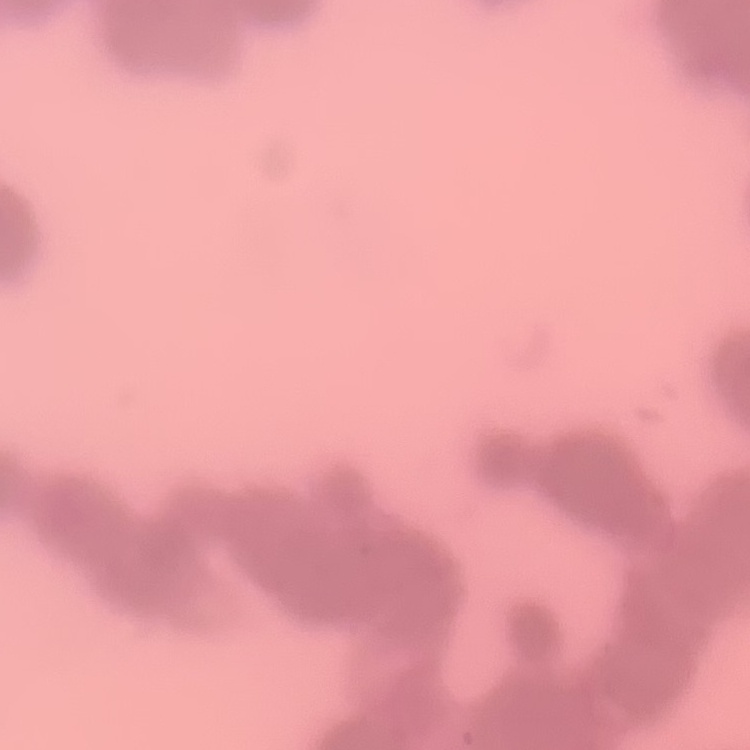

Summary:
  - Erythrocyte morphology: rouleaux formation
  - Stain: Field's or Giemsa
  - Image type: one tile cut from a larger photomicrograph
  - Preparation: thin peripheral smear